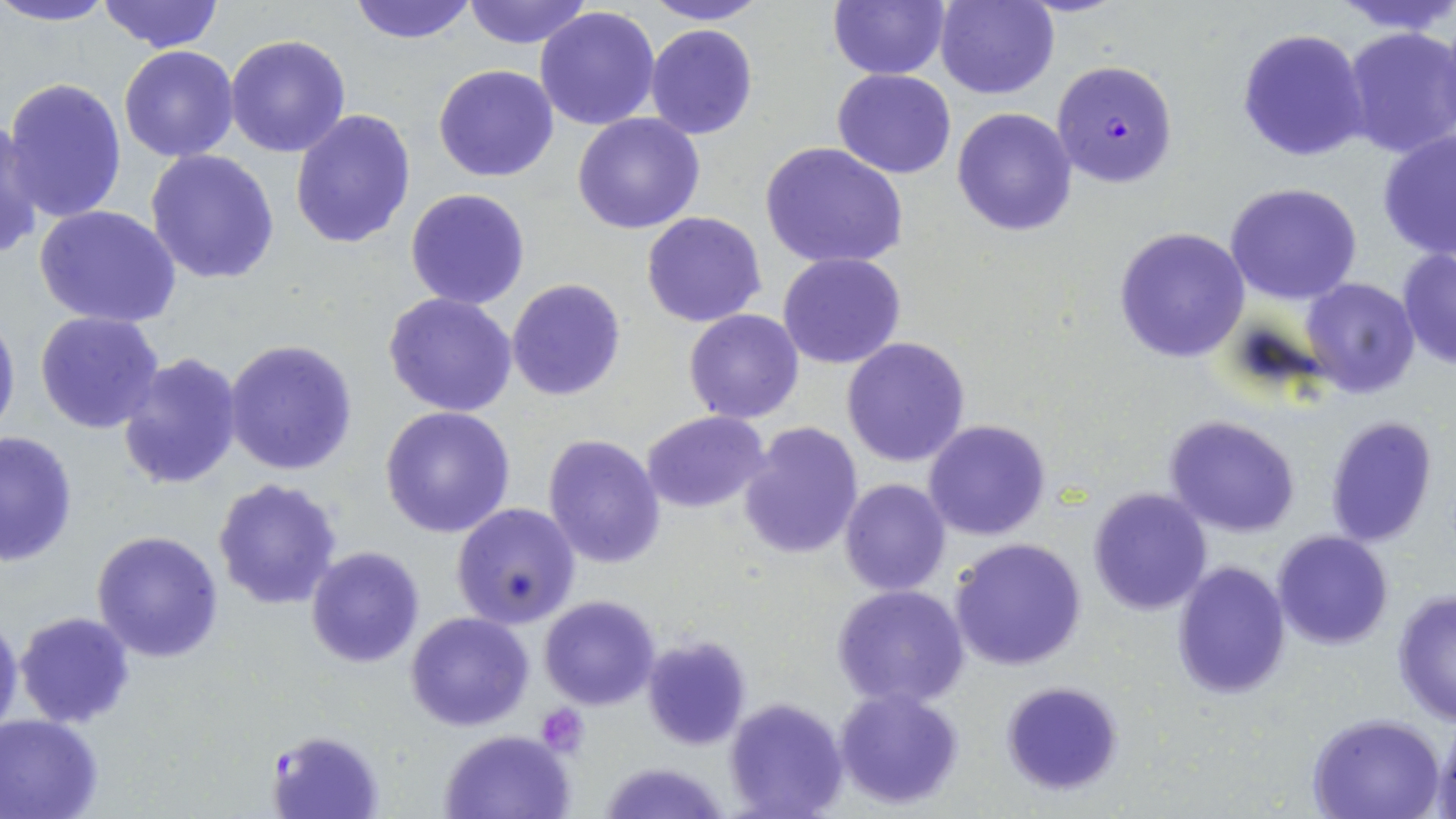 Approximate bounding boxes as named x1/y1/x2/y2 corners in pixels. Plasmodium falciparum-infected red blood cell locations: (x1=1052, y1=59, x2=1177, y2=188), (x1=267, y1=731, x2=382, y2=816). Platelet locations: (x1=538, y1=704, x2=592, y2=755). Uninfected red blood cell locations: (x1=0, y1=0, x2=117, y2=27), (x1=97, y1=0, x2=224, y2=53), (x1=462, y1=0, x2=593, y2=48), (x1=641, y1=0, x2=771, y2=25), (x1=827, y1=0, x2=949, y2=79), (x1=935, y1=0, x2=1058, y2=99), (x1=1333, y1=0, x2=1456, y2=36), (x1=345, y1=1, x2=479, y2=45), (x1=534, y1=6, x2=661, y2=131), (x1=645, y1=23, x2=760, y2=141), (x1=1340, y1=26, x2=1456, y2=161), (x1=1236, y1=28, x2=1369, y2=162), (x1=223, y1=33, x2=351, y2=157), (x1=117, y1=46, x2=241, y2=162), (x1=433, y1=65, x2=559, y2=182), (x1=833, y1=68, x2=955, y2=178), (x1=4, y1=77, x2=127, y2=222), (x1=289, y1=107, x2=416, y2=250), (x1=952, y1=107, x2=1077, y2=235), (x1=572, y1=112, x2=706, y2=235), (x1=0, y1=122, x2=42, y2=262), (x1=1377, y1=127, x2=1456, y2=262), (x1=759, y1=142, x2=908, y2=271), (x1=145, y1=149, x2=280, y2=285), (x1=1225, y1=181, x2=1363, y2=305), (x1=405, y1=188, x2=531, y2=310), (x1=34, y1=203, x2=182, y2=328), (x1=642, y1=212, x2=767, y2=328), (x1=1114, y1=226, x2=1252, y2=364), (x1=1397, y1=248, x2=1456, y2=369), (x1=778, y1=252, x2=907, y2=370), (x1=1301, y1=276, x2=1422, y2=398), (x1=506, y1=278, x2=626, y2=401), (x1=383, y1=292, x2=519, y2=419), (x1=0, y1=306, x2=20, y2=444), (x1=683, y1=309, x2=804, y2=424), (x1=34, y1=310, x2=166, y2=435), (x1=841, y1=337, x2=971, y2=468), (x1=222, y1=339, x2=359, y2=475), (x1=115, y1=351, x2=242, y2=490), (x1=379, y1=406, x2=516, y2=539), (x1=642, y1=410, x2=772, y2=514), (x1=1163, y1=413, x2=1302, y2=538), (x1=1323, y1=414, x2=1437, y2=548), (x1=922, y1=418, x2=1053, y2=541), (x1=737, y1=421, x2=863, y2=560), (x1=1, y1=430, x2=77, y2=567), (x1=542, y1=434, x2=666, y2=569), (x1=213, y1=476, x2=344, y2=610), (x1=840, y1=479, x2=952, y2=598), (x1=1087, y1=488, x2=1213, y2=615), (x1=451, y1=502, x2=580, y2=628), (x1=1271, y1=529, x2=1393, y2=650), (x1=91, y1=530, x2=224, y2=664), (x1=949, y1=537, x2=1088, y2=671), (x1=305, y1=545, x2=427, y2=668), (x1=1172, y1=561, x2=1290, y2=700), (x1=830, y1=585, x2=971, y2=711), (x1=1391, y1=590, x2=1456, y2=726), (x1=539, y1=595, x2=660, y2=710), (x1=0, y1=610, x2=24, y2=742), (x1=13, y1=610, x2=137, y2=729), (x1=405, y1=611, x2=534, y2=732), (x1=642, y1=634, x2=751, y2=750), (x1=1001, y1=681, x2=1125, y2=798), (x1=833, y1=688, x2=965, y2=809), (x1=723, y1=696, x2=849, y2=819), (x1=0, y1=713, x2=107, y2=819), (x1=1308, y1=713, x2=1446, y2=819), (x1=1436, y1=719, x2=1456, y2=818), (x1=439, y1=728, x2=576, y2=818), (x1=597, y1=759, x2=733, y2=818). Slide-level diagnosis: Plasmodium falciparum. Single field of view. May-Grünwald-Giemsa stain. Thin blood film. Image is 1456×819 pixels. Optical microscopy. Captured at 1000x magnification.